Report the malaria status of this cell.
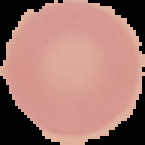
Uninfected.

Summary:
  - Image size: 145×145 pixels
  - Preparation: thin blood smear
  - Image type: segmented cell region on a black background